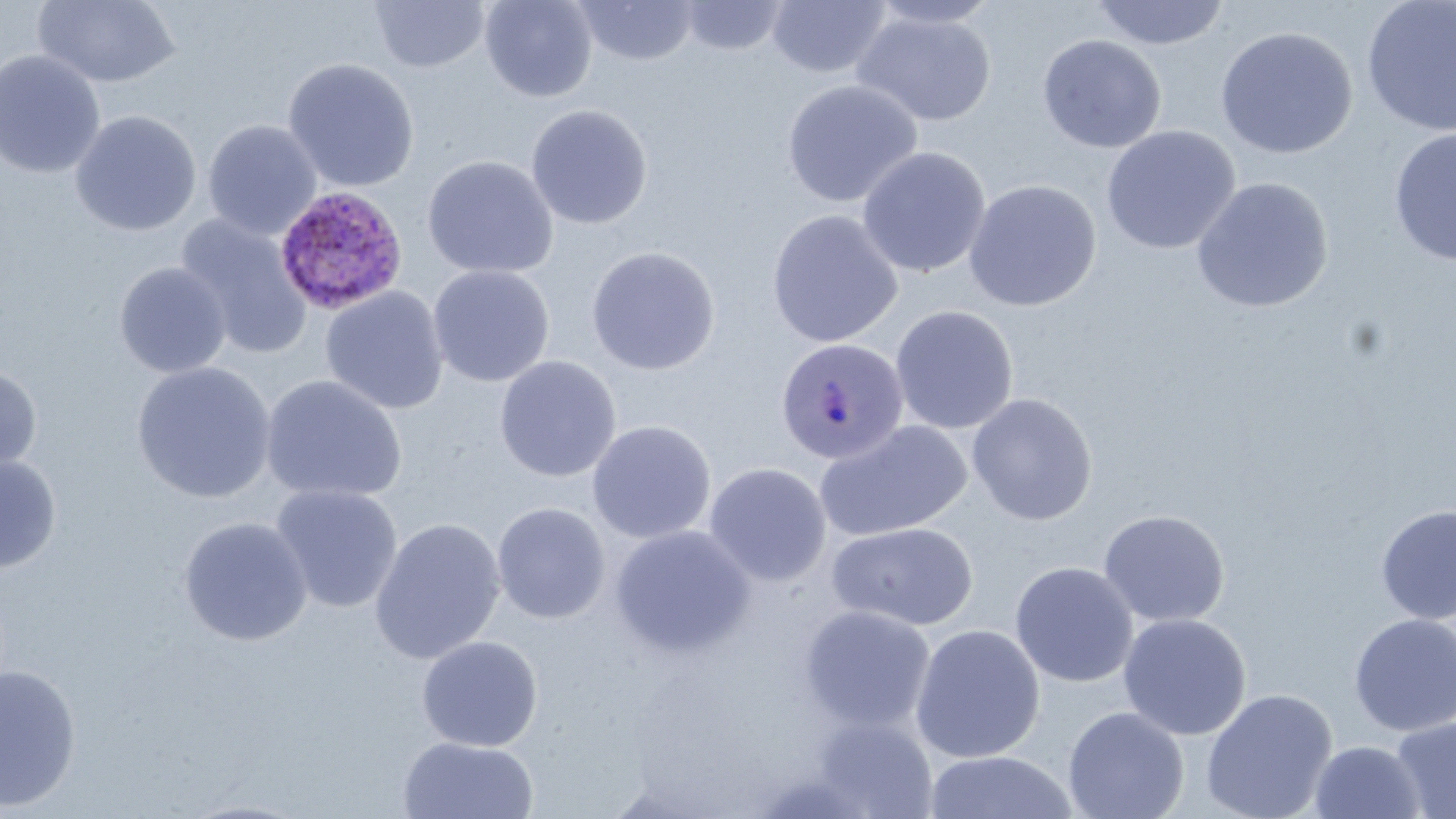

slide-level diagnosis = Plasmodium ovale
magnification = 1000x
preparation = thin blood film
image size = 1456×819 pixels
field of view = one of a larger specimen
modality = optical microscopy
uninfected red blood cell locations = approximate bounding boxes as [x1, y1, x2, y2] in pixels: [33, 0, 182, 88], [369, 0, 490, 73], [480, 0, 597, 102], [572, 0, 699, 66], [679, 0, 789, 56], [867, 0, 1003, 29], [1090, 0, 1230, 50], [1361, 0, 1456, 137], [766, 1, 891, 79], [853, 10, 996, 126], [1215, 25, 1358, 159], [1037, 34, 1167, 153], [0, 49, 106, 179], [282, 57, 420, 192], [782, 78, 923, 208], [526, 104, 653, 229], [70, 110, 202, 237], [203, 119, 322, 239], [1100, 125, 1241, 254], [1388, 128, 1456, 266], [856, 146, 992, 278], [421, 154, 559, 279], [1191, 177, 1333, 313], [963, 179, 1102, 312], [766, 209, 904, 348], [176, 213, 313, 359], [585, 245, 721, 375], [114, 261, 231, 378], [428, 264, 555, 388], [319, 287, 449, 415], [890, 305, 1019, 434], [494, 355, 621, 483], [132, 361, 276, 504], [0, 363, 43, 480], [261, 375, 407, 504], [966, 393, 1098, 525], [587, 420, 716, 543], [815, 420, 973, 542], [0, 453, 62, 574], [703, 462, 832, 587], [269, 484, 404, 613], [492, 502, 611, 624], [1375, 504, 1456, 624], [1097, 509, 1230, 627], [178, 516, 313, 646], [368, 517, 505, 665], [826, 522, 979, 631], [610, 525, 756, 659], [1009, 561, 1138, 688], [798, 605, 936, 733], [1118, 613, 1252, 740], [1348, 613, 1456, 736], [910, 623, 1046, 763], [416, 635, 543, 752], [0, 665, 82, 812], [1201, 688, 1338, 819], [1062, 706, 1189, 819], [813, 715, 938, 818], [1389, 716, 1456, 818], [397, 736, 539, 818], [1309, 740, 1426, 818], [925, 750, 1078, 819], [176, 798, 314, 819]
Plasmodium ovale-infected red blood cell locations = approximate bounding boxes as [x1, y1, x2, y2] in pixels: [273, 184, 409, 315], [775, 337, 910, 465]
stain = May-Grünwald-Giemsa